Report the malaria status of this cell.
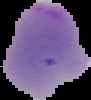

It is uninfected.

image_size: 91×100 pixels
image_type: segmented cell region with the area outside set to black
preparation: thin blood film